Describe the morphology of the erythrocytes.
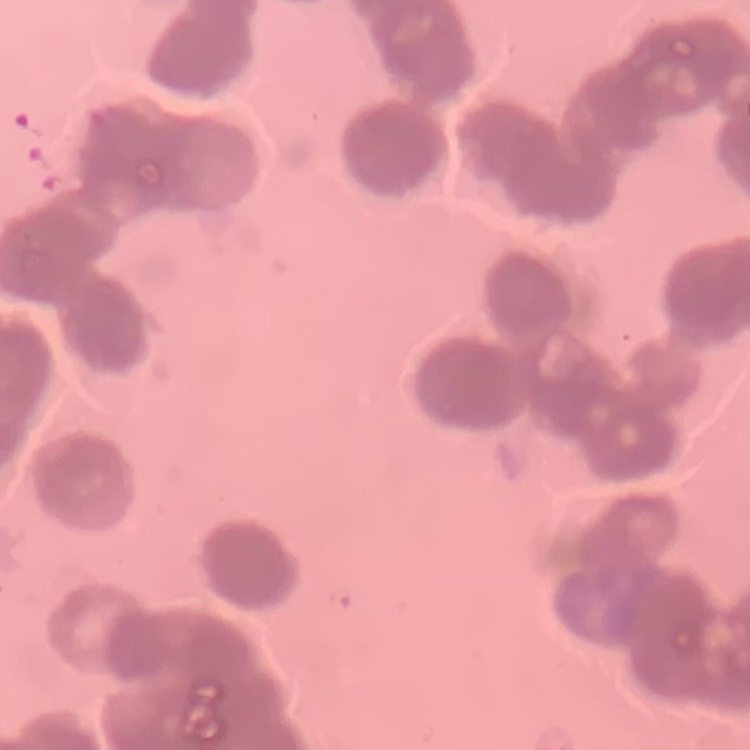
Rouleaux formation.

Thin peripheral smear. Stained with either Field's or Giemsa. Square crop of a larger photomicrograph.